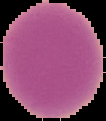

Summary:
  - Image size: 106×121 pixels
  - Malaria status: uninfected
  - Preparation: thin blood smear
  - Image type: segmented cell region with the area outside set to black